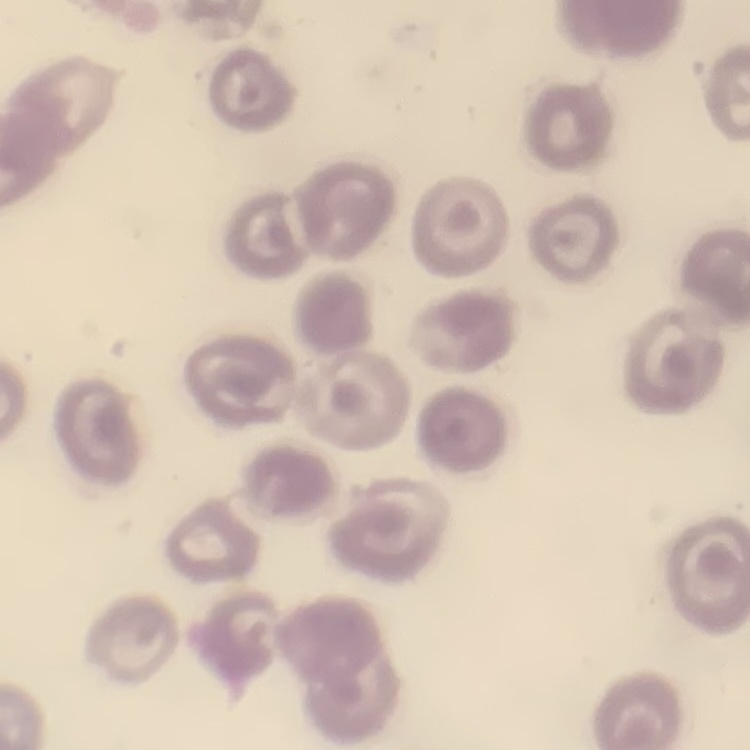
Summary:
  - Red blood cell morphology: no rouleaux formation
  - Stain: Field's or Giemsa
  - Image type: one tile cut from a larger photomicrograph
  - Preparation: thin peripheral smear